Draw a bounding box around every malaria parasite, every leukocyte, and every artifact (stain precipitate or debris).
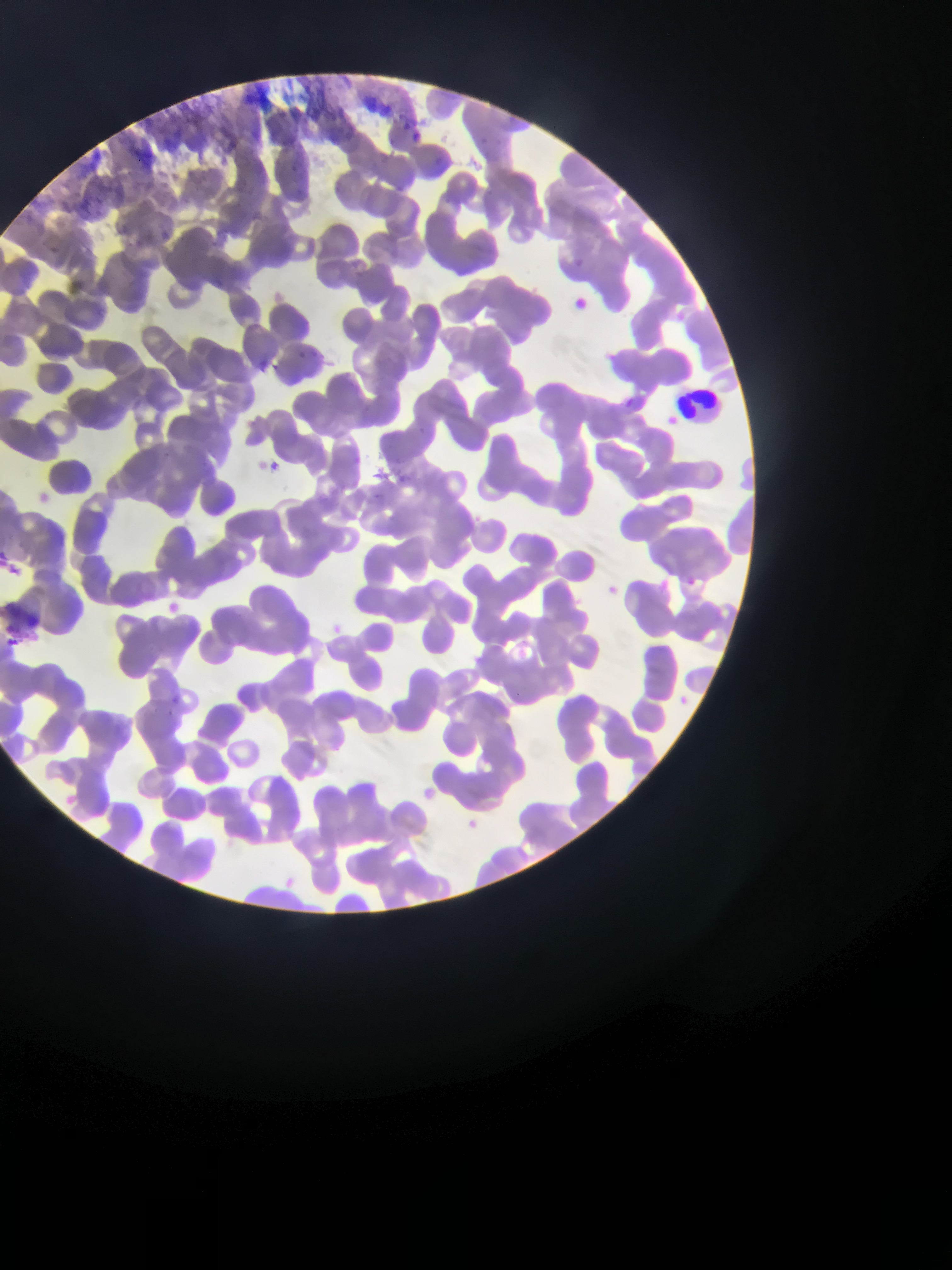
Approximate bounding boxes as (left, top, right, bottom) in pixels.
No malaria parasites observed.
Leukocytes: (672, 386, 733, 430).

One field of view. Thin blood film. Collected in Ghana. Mobile-phone photograph taken through the microscope. Image is 952×1270 pixels.